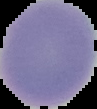
image_type: segmented cell region on a black background
preparation: thin blood smear
malaria_status: uninfected
image_size: 97×109 pixels